Report the malaria status of this cell.
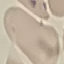

It is uninfected.

Photographed with a smartphone camera at the microscope eyepiece. Thin blood film. Automatically extracted cell patch, resized to 64 × 64 pixels. Giemsa-stained preparation.